Point out each Plasmodium parasite.
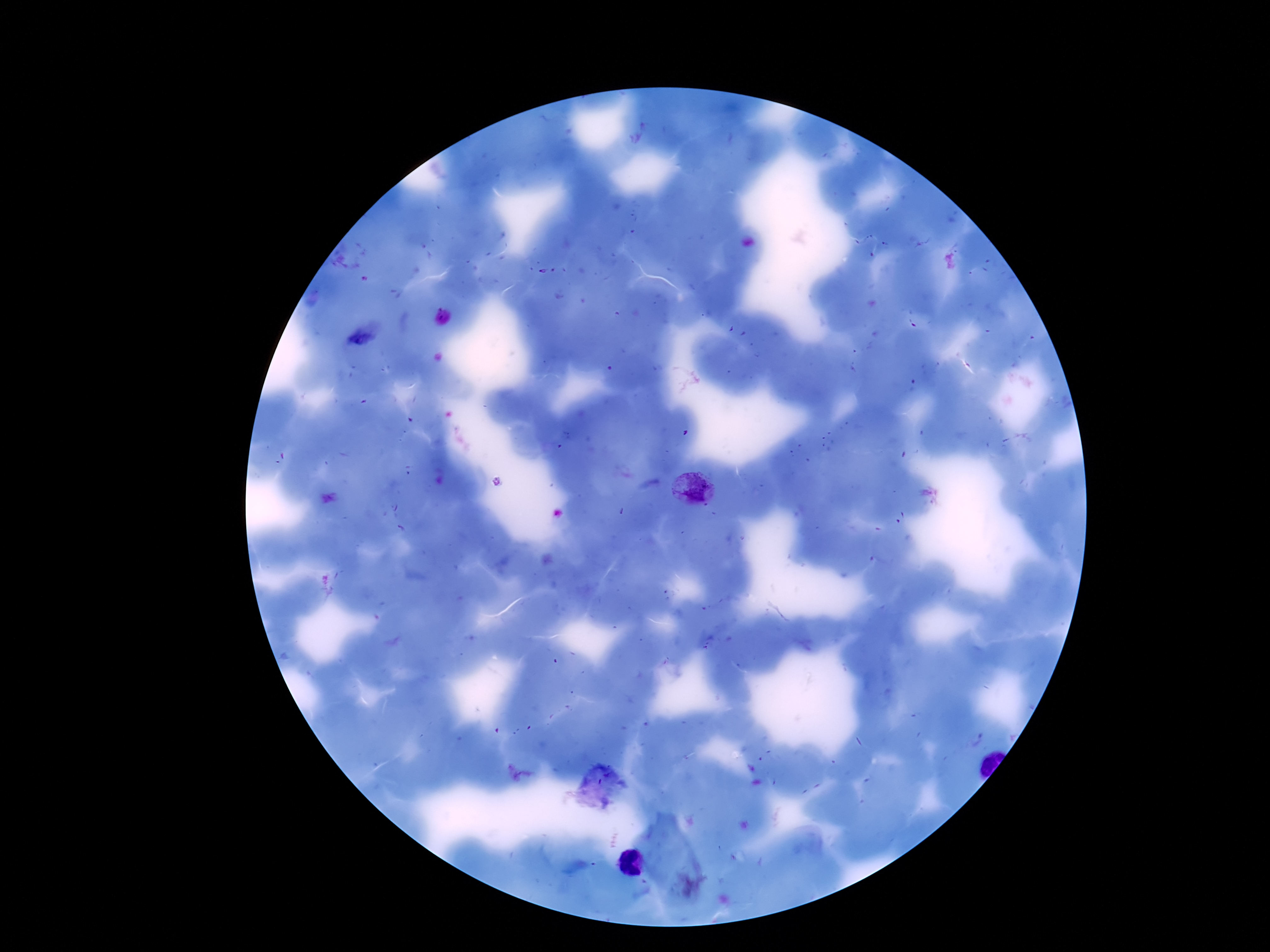
Approximate centers as {x, y} in pixels.
Plasmodium parasites: {694, 489}.

Summary:
  - Stain: Giemsa
  - Capture: smartphone camera through the microscope eyepiece
  - Magnification: 100x
  - Image size: 1270×952 pixels
  - Patient malaria status: positive
  - Field of view: single
  - Preparation: thick blood film